Report the malaria status of this cell.
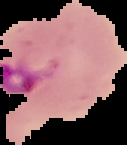

Parasitized.

Summary:
  - Image type: cell region segmented out of the field of view; surrounding area masked to black
  - Image size: 127×145 pixels
  - Preparation: thin blood film